Comment on the morphology of the erythrocytes.
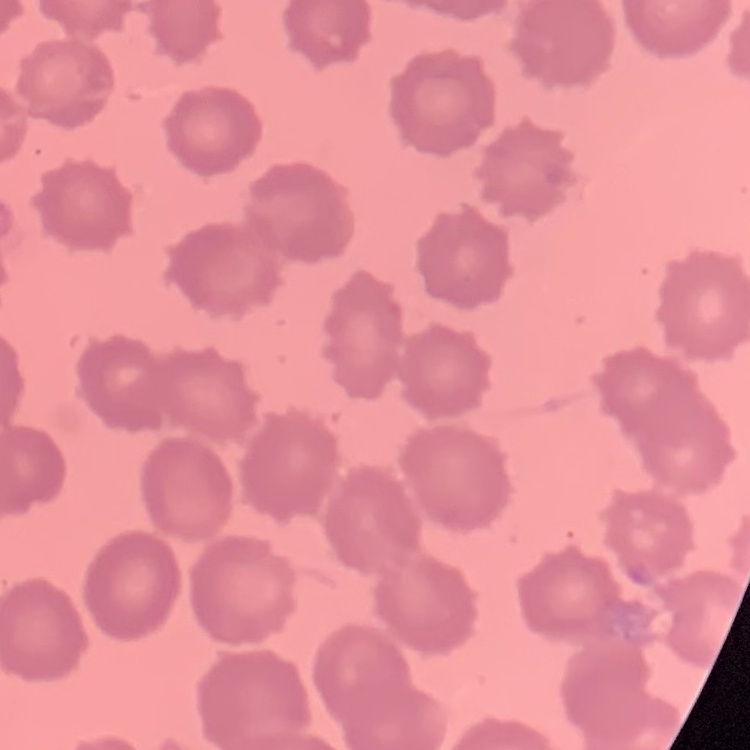

They show no rouleaux formation.

image_type: one tile cut from a larger photomicrograph
preparation: thin peripheral smear
stain: Field's or Giemsa